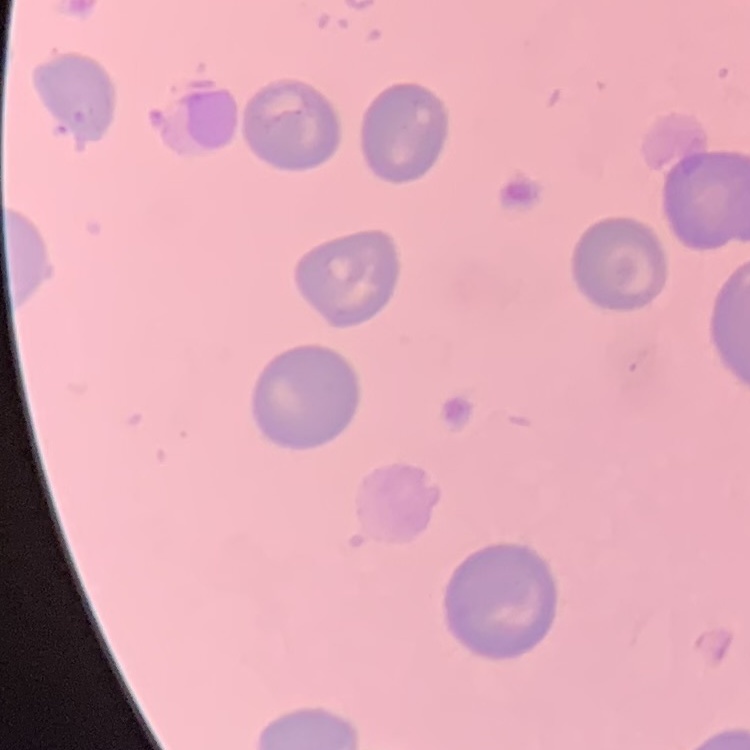

red blood cell morphology = no rouleaux formation
stain = Field's or Giemsa
preparation = thin blood smear
image type = square crop of a larger photomicrograph